Report the malaria status of this cell.
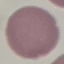
It is uninfected.

Summary:
  - Capture: smartphone through the microscope eyepiece
  - Image type: cell patch, automatically extracted from a larger field of view and resized to 64 × 64 pixels
  - Stain: Giemsa
  - Preparation: thin blood film